Classify this cell by malaria status.
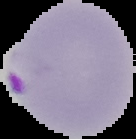

It is parasitized.

Summary:
  - Image type: segmented cell region with the area outside set to black
  - Image size: 136×139 pixels
  - Preparation: thin blood smear